Give the position of every Plasmodium parasite visible.
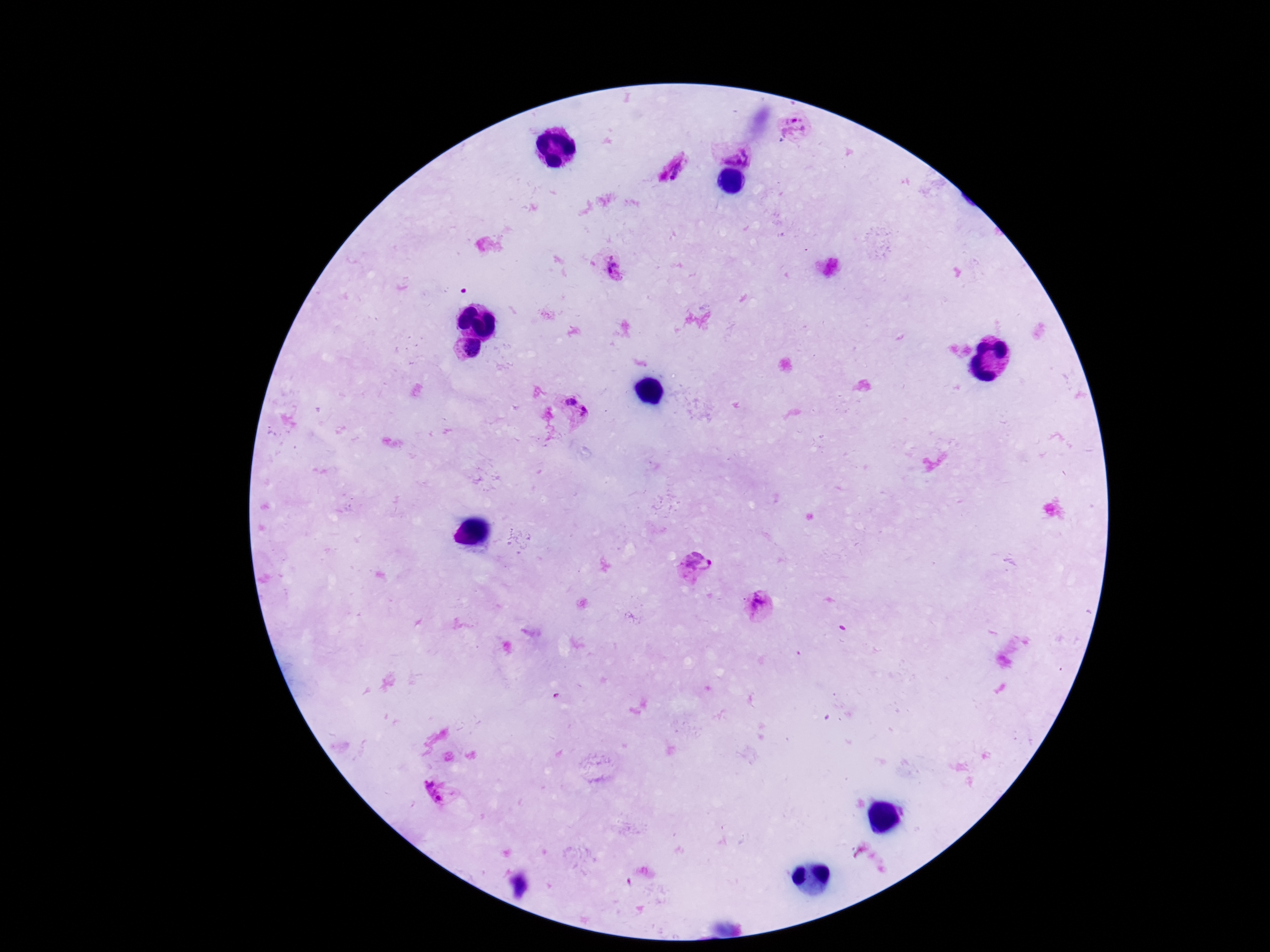

Approximate centers as [x, y] in pixels.
Plasmodium parasites: [795, 128], [732, 152], [672, 169], [608, 267], [466, 348], [565, 393], [583, 416], [693, 568], [761, 607], [433, 795].

Patient malaria status: infected. Giemsa-stained preparation. 100x magnification. Smartphone photograph taken through the microscope eyepiece. Thick peripheral-blood smear. Image is 1270×952 pixels. One field from this slide.